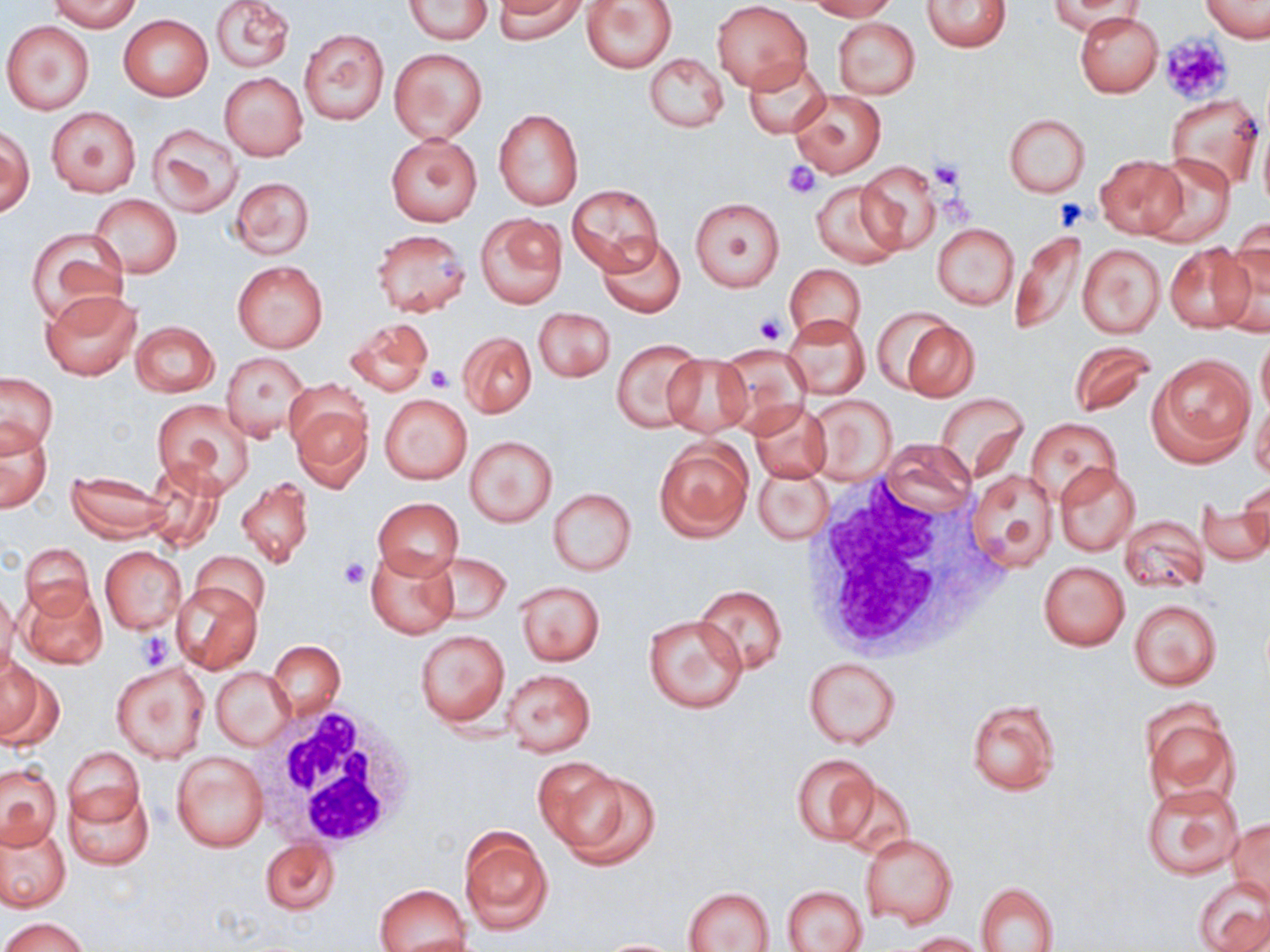
Approximate bounding boxes as [x1, y1, x2, y2] in pixels. Uninfected red blood cell locations (subset): [50, 0, 139, 32], [210, 0, 294, 74], [405, 0, 490, 43], [494, 0, 584, 43], [581, 0, 677, 73], [806, 0, 896, 20], [1201, 0, 1269, 43], [921, 1, 1013, 53], [1048, 1, 1145, 35], [711, 2, 812, 91], [1073, 11, 1163, 97], [118, 14, 213, 101], [832, 17, 920, 99], [2, 19, 97, 116], [298, 28, 390, 125], [389, 48, 488, 145], [644, 53, 729, 133], [742, 58, 830, 137], [220, 72, 307, 160], [790, 89, 885, 177], [1165, 93, 1264, 193], [45, 106, 141, 198], [494, 109, 584, 211], [1004, 114, 1090, 197], [147, 122, 245, 216], [1, 127, 34, 215], [385, 135, 482, 227], [1142, 152, 1237, 248], [1095, 155, 1187, 240], [856, 161, 943, 254], [230, 176, 315, 259], [811, 180, 904, 269], [567, 183, 664, 273], [90, 195, 183, 278], [691, 198, 784, 291], [476, 214, 567, 308], [931, 222, 1019, 310], [27, 228, 127, 325], [1011, 228, 1090, 337], [371, 229, 471, 316], [596, 232, 686, 318], [1214, 235, 1270, 336], [1076, 242, 1166, 339], [1165, 243, 1254, 334], [232, 259, 329, 352], [785, 265, 866, 340], [41, 289, 141, 381], [534, 309, 614, 382], [781, 314, 869, 401], [893, 315, 980, 402], [345, 318, 434, 397], [131, 321, 219, 398], [457, 331, 537, 417], [1257, 331, 1270, 418], [610, 340, 704, 431], [1067, 342, 1158, 418], [713, 343, 813, 431], [223, 352, 310, 441], [661, 353, 752, 438], [1149, 355, 1255, 466], [0, 373, 57, 453], [935, 392, 1029, 480], [380, 393, 472, 484], [805, 394, 899, 485], [1249, 394, 1270, 481], [290, 398, 373, 492], [151, 399, 253, 494], [746, 400, 832, 484], [1026, 418, 1121, 502], [0, 421, 53, 513], [464, 434, 557, 527], [653, 438, 754, 541], [879, 440, 979, 517], [141, 461, 229, 552], [1054, 462, 1138, 555], [754, 464, 832, 545], [965, 468, 1059, 571], [66, 472, 171, 541], [237, 477, 313, 567], [1238, 480, 1269, 555], [547, 488, 636, 576], [371, 499, 463, 578], [1198, 499, 1270, 566], [1118, 514, 1210, 593], [21, 543, 95, 618], [366, 545, 460, 639], [100, 546, 186, 633], [191, 551, 271, 622], [426, 553, 509, 624], [1037, 562, 1129, 650], [170, 580, 262, 674], [514, 580, 605, 666], [20, 584, 108, 670], [692, 584, 788, 674], [0, 586, 19, 682], [1129, 600, 1222, 691], [643, 615, 747, 714], [415, 628, 510, 728], [268, 640, 345, 720], [802, 656, 902, 750], [0, 657, 62, 746], [111, 661, 210, 763], [211, 666, 295, 751], [502, 668, 596, 756], [966, 697, 1062, 797], [1140, 699, 1238, 811], [64, 747, 144, 832], [171, 749, 269, 851], [792, 753, 878, 846], [537, 762, 657, 867], [0, 763, 62, 848], [832, 776, 917, 861], [65, 782, 152, 869], [1142, 783, 1244, 880], [1227, 818, 1269, 904], [0, 819, 71, 913], [458, 823, 553, 936], [859, 832, 958, 929], [260, 837, 341, 916], [1193, 876, 1270, 952], [976, 881, 1059, 952], [374, 883, 470, 952], [782, 885, 870, 952], [682, 886, 776, 952], [3, 917, 88, 952], [906, 932, 987, 951], [593, 938, 689, 952]. Platelet locations: [1159, 34, 1233, 106], [929, 160, 967, 194], [783, 161, 822, 197], [1054, 198, 1091, 230], [755, 313, 786, 345], [428, 367, 453, 392], [338, 557, 369, 589], [138, 632, 171, 668]. White blood cell locations (subset): [261, 700, 420, 854]. Slide-level diagnosis: no evidence of blood parasites. May-Grünwald-Giemsa-stained preparation. Image is 1270×952 pixels. Light microscopy. One field of a larger specimen. Thin blood smear. 1000x magnification.